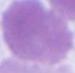
Summary:
  - Identification: red blood cell
  - Magnification: 1000x
  - Modality: photomicrograph